Identify the blood parasite species.
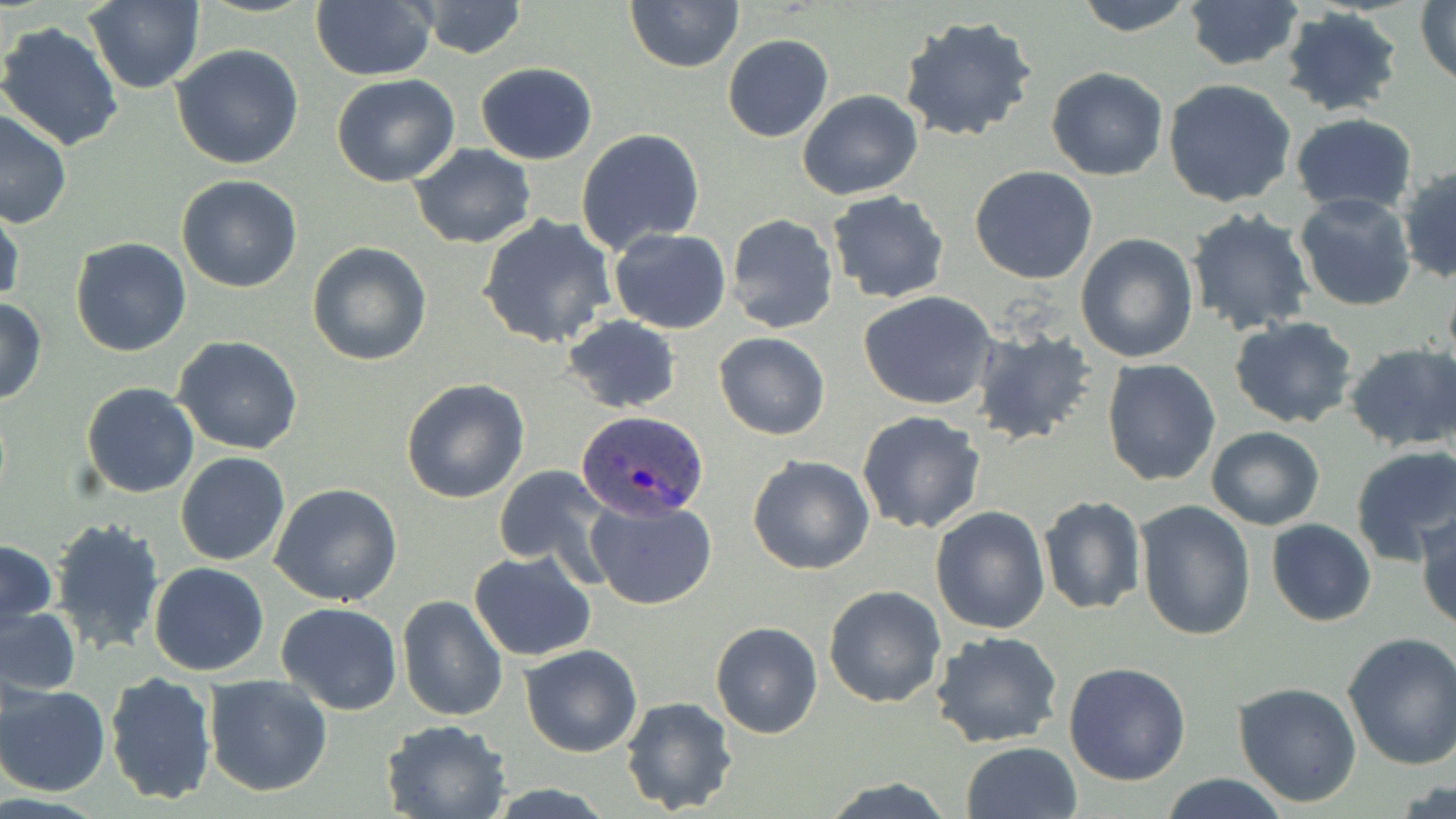
Plasmodium ovale.

Summary:
  - Coordinate format: approximate bounding boxes as (x1, y1, x2, y2) in pixels
  - Plasmodium ovale-infected red blood cell locations: (573, 411, 709, 522)
  - Uninfected red blood cell locations: (311, 0, 435, 81), (624, 0, 744, 73), (1070, 0, 1199, 36), (1181, 0, 1305, 73), (84, 1, 203, 94), (415, 1, 527, 59), (1416, 1, 1456, 87), (1278, 6, 1402, 118), (898, 16, 1039, 144), (0, 21, 124, 153), (722, 34, 833, 142), (172, 43, 305, 170), (476, 62, 597, 164), (1046, 67, 1169, 181), (331, 75, 460, 187), (1163, 80, 1298, 209), (797, 89, 924, 201), (0, 110, 73, 229), (1290, 112, 1418, 217), (577, 128, 706, 254), (409, 143, 537, 249), (1397, 164, 1456, 284), (969, 165, 1098, 284), (177, 173, 305, 292), (825, 190, 951, 306), (1293, 191, 1418, 312), (0, 199, 23, 309), (1184, 208, 1315, 336), (725, 213, 839, 335), (476, 214, 617, 350), (609, 228, 732, 335), (1075, 233, 1199, 363), (70, 237, 192, 357), (307, 242, 432, 367), (859, 290, 999, 411), (0, 298, 48, 405), (563, 314, 682, 414), (1228, 317, 1358, 429), (970, 325, 1100, 447), (713, 332, 831, 440), (174, 336, 304, 455), (1343, 343, 1456, 453), (1100, 358, 1221, 487), (401, 378, 530, 503), (80, 381, 199, 499), (856, 410, 987, 534), (1206, 426, 1324, 530), (1349, 445, 1456, 566), (176, 452, 289, 567), (747, 454, 875, 575), (492, 463, 613, 576), (270, 484, 404, 607), (1037, 492, 1146, 618), (584, 496, 717, 610), (1136, 500, 1257, 641), (931, 506, 1050, 633), (1416, 509, 1456, 631), (49, 516, 165, 656), (1267, 520, 1376, 626), (1, 540, 56, 628), (468, 551, 597, 660), (149, 562, 269, 676), (823, 585, 946, 709), (396, 594, 507, 723), (0, 603, 80, 696), (275, 603, 401, 714), (710, 621, 823, 739), (931, 632, 1063, 750), (1341, 633, 1456, 770), (519, 644, 643, 758), (1063, 661, 1192, 786), (103, 671, 217, 805), (203, 675, 333, 797), (1, 683, 109, 796), (1232, 683, 1363, 807), (619, 696, 740, 817), (381, 718, 513, 819), (960, 741, 1083, 819), (1158, 773, 1290, 819), (819, 778, 957, 817)
  - Field of view: one of a larger specimen
  - Modality: light microscopy
  - Image size: 1456×819 pixels
  - Preparation: thin blood film
  - Magnification: 1000x
  - Stain: May-Grünwald-Giemsa